Comment on the morphology of the red blood cells.
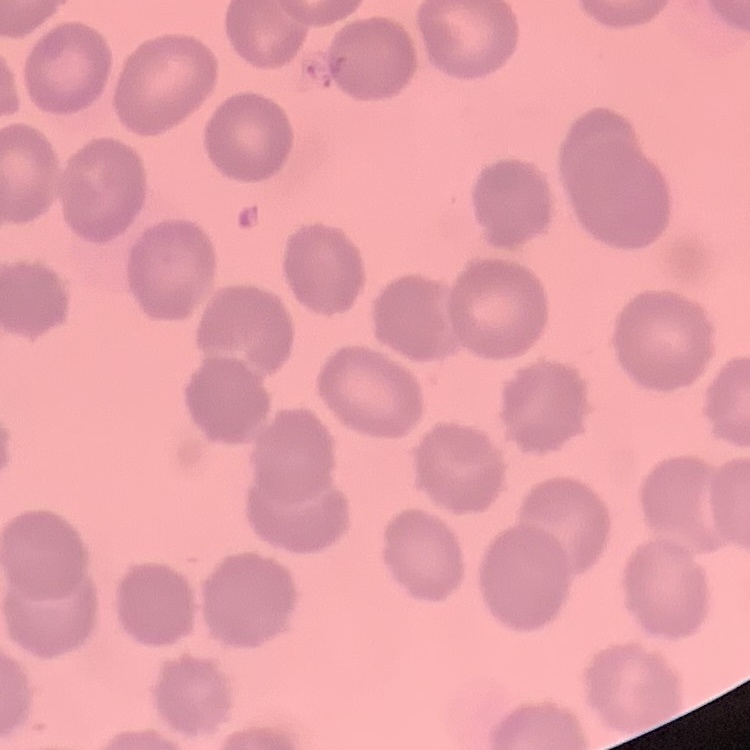
No rouleaux formation.

stain = Field's or Giemsa
image type = one tile cut from a larger photomicrograph
preparation = thin blood smear